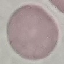
malaria status = uninfected
capture = smartphone camera at the microscope eyepiece
preparation = thin blood smear
image type = automatically extracted cell patch, resized to 64 × 64 pixels
stain = Giemsa